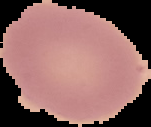

Summary:
  - Result: no malaria parasites detected
  - Preparation: thin blood smear
  - Image type: segmented cell region with the area outside set to black
  - Image size: 151×127 pixels